Identify the cell.
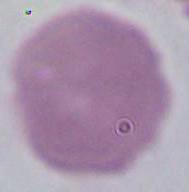

An erythrocyte.

1000x magnification. Photomicrograph.